Report the malaria status of this cell.
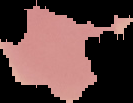

It is uninfected.

Summary:
  - Image size: 133×103 pixels
  - Image type: segmented cell region on a black background
  - Preparation: thin blood smear